Assess this cell for malaria.
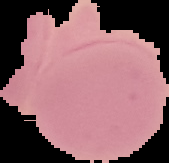

Uninfected.

{
  "image_type": "segmented cell region with the area outside set to black",
  "preparation": "thin blood smear",
  "image_size": "169×163 pixels"
}